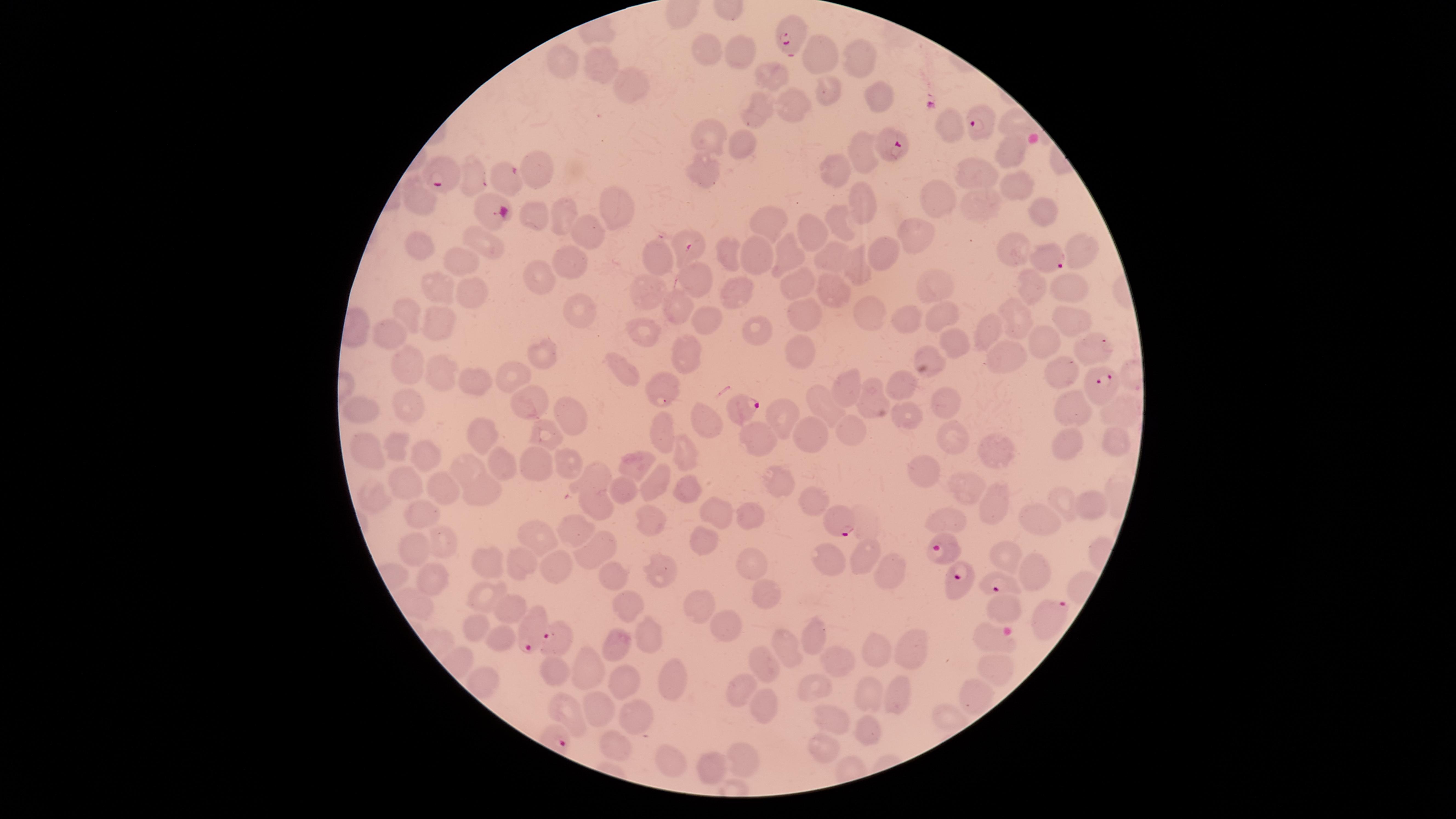 Approximate marker points, in pixels from the top-left corner. Uninfected red blood cells: (x=706, y=49), (x=741, y=54), (x=826, y=55), (x=860, y=55), (x=558, y=56), (x=599, y=57), (x=625, y=74), (x=776, y=76), (x=833, y=87), (x=880, y=99), (x=788, y=106), (x=759, y=109), (x=948, y=121), (x=710, y=134), (x=741, y=142), (x=858, y=151), (x=1013, y=151), (x=542, y=160), (x=702, y=174), (x=833, y=175), (x=973, y=175), (x=473, y=176), (x=1015, y=184), (x=427, y=198), (x=937, y=200), (x=986, y=204), (x=612, y=205), (x=862, y=205), (x=1038, y=209), (x=565, y=212), (x=533, y=213), (x=843, y=224), (x=591, y=226), (x=767, y=227), (x=921, y=233), (x=815, y=234), (x=483, y=240), (x=422, y=241), (x=725, y=248), (x=1016, y=249), (x=1085, y=249), (x=653, y=253), (x=756, y=253), (x=882, y=255), (x=789, y=256), (x=836, y=257), (x=570, y=258), (x=457, y=261), (x=857, y=269), (x=701, y=275), (x=541, y=277), (x=800, y=282), (x=1032, y=282), (x=936, y=283), (x=438, y=288), (x=1072, y=289), (x=648, y=290), (x=830, y=290), (x=743, y=293), (x=473, y=294), (x=579, y=308), (x=802, y=308), (x=680, y=311), (x=868, y=313), (x=409, y=314), (x=938, y=315), (x=1072, y=316), (x=440, y=320), (x=908, y=320), (x=706, y=322), (x=1020, y=322), (x=993, y=329), (x=760, y=330), (x=391, y=332), (x=641, y=333), (x=1043, y=340), (x=952, y=341), (x=1093, y=350), (x=1009, y=352), (x=932, y=353), (x=547, y=354), (x=802, y=356), (x=690, y=359), (x=410, y=366), (x=443, y=373), (x=512, y=374), (x=625, y=374), (x=1061, y=376), (x=468, y=379), (x=663, y=381), (x=902, y=383), (x=856, y=390), (x=529, y=396), (x=877, y=401), (x=945, y=403), (x=411, y=404), (x=824, y=406), (x=361, y=408), (x=1078, y=409), (x=1124, y=410), (x=905, y=414), (x=780, y=415), (x=574, y=417), (x=707, y=420), (x=659, y=429), (x=851, y=431), (x=546, y=433), (x=953, y=434), (x=760, y=436), (x=487, y=437), (x=811, y=437), (x=1112, y=439), (x=1066, y=442), (x=402, y=445), (x=369, y=448), (x=680, y=450), (x=1001, y=450), (x=417, y=455), (x=566, y=463), (x=638, y=464), (x=531, y=465), (x=503, y=468), (x=472, y=471), (x=927, y=471), (x=600, y=477), (x=775, y=479), (x=660, y=481), (x=411, y=485), (x=687, y=486), (x=623, y=487), (x=484, y=489), (x=443, y=491), (x=965, y=493), (x=382, y=494), (x=1000, y=499), (x=1065, y=499), (x=815, y=500), (x=595, y=501), (x=1087, y=501), (x=710, y=511), (x=750, y=515), (x=1037, y=516), (x=651, y=518), (x=422, y=519), (x=946, y=523), (x=581, y=526), (x=536, y=538), (x=703, y=539), (x=600, y=544), (x=442, y=546), (x=418, y=549), (x=1008, y=553), (x=866, y=558), (x=829, y=559), (x=754, y=562), (x=493, y=566), (x=523, y=566), (x=554, y=568), (x=1030, y=568), (x=663, y=569), (x=616, y=573), (x=895, y=576), (x=432, y=577), (x=763, y=594), (x=489, y=597), (x=703, y=602), (x=629, y=606), (x=509, y=611), (x=1005, y=611), (x=729, y=624), (x=477, y=630), (x=648, y=631), (x=817, y=637), (x=499, y=638), (x=991, y=639), (x=783, y=643), (x=617, y=644), (x=912, y=648), (x=876, y=656), (x=846, y=660), (x=591, y=661), (x=1003, y=664), (x=764, y=667), (x=557, y=672), (x=667, y=680), (x=742, y=682), (x=627, y=685), (x=819, y=690), (x=897, y=691), (x=872, y=693), (x=974, y=697), (x=566, y=706), (x=598, y=708), (x=767, y=708), (x=945, y=718), (x=836, y=721), (x=639, y=722), (x=861, y=730), (x=822, y=745), (x=623, y=751), (x=746, y=757), (x=667, y=762), (x=708, y=768). Parasitized red blood cells: (x=794, y=32), (x=977, y=128), (x=886, y=144), (x=440, y=172), (x=506, y=178), (x=494, y=208), (x=689, y=245), (x=1053, y=262), (x=1106, y=388), (x=739, y=404), (x=835, y=519), (x=944, y=548), (x=999, y=584), (x=960, y=585), (x=1046, y=619), (x=530, y=628), (x=557, y=638). Circular visible region. Image is 1456×819 pixels. Giemsa stain. Species: Plasmodium falciparum. Single field of view. Thin blood film. Presence: malaria parasites seen. Smartphone photograph through the microscope eyepiece.